Locate every Plasmodium falciparum-infected red blood cell.
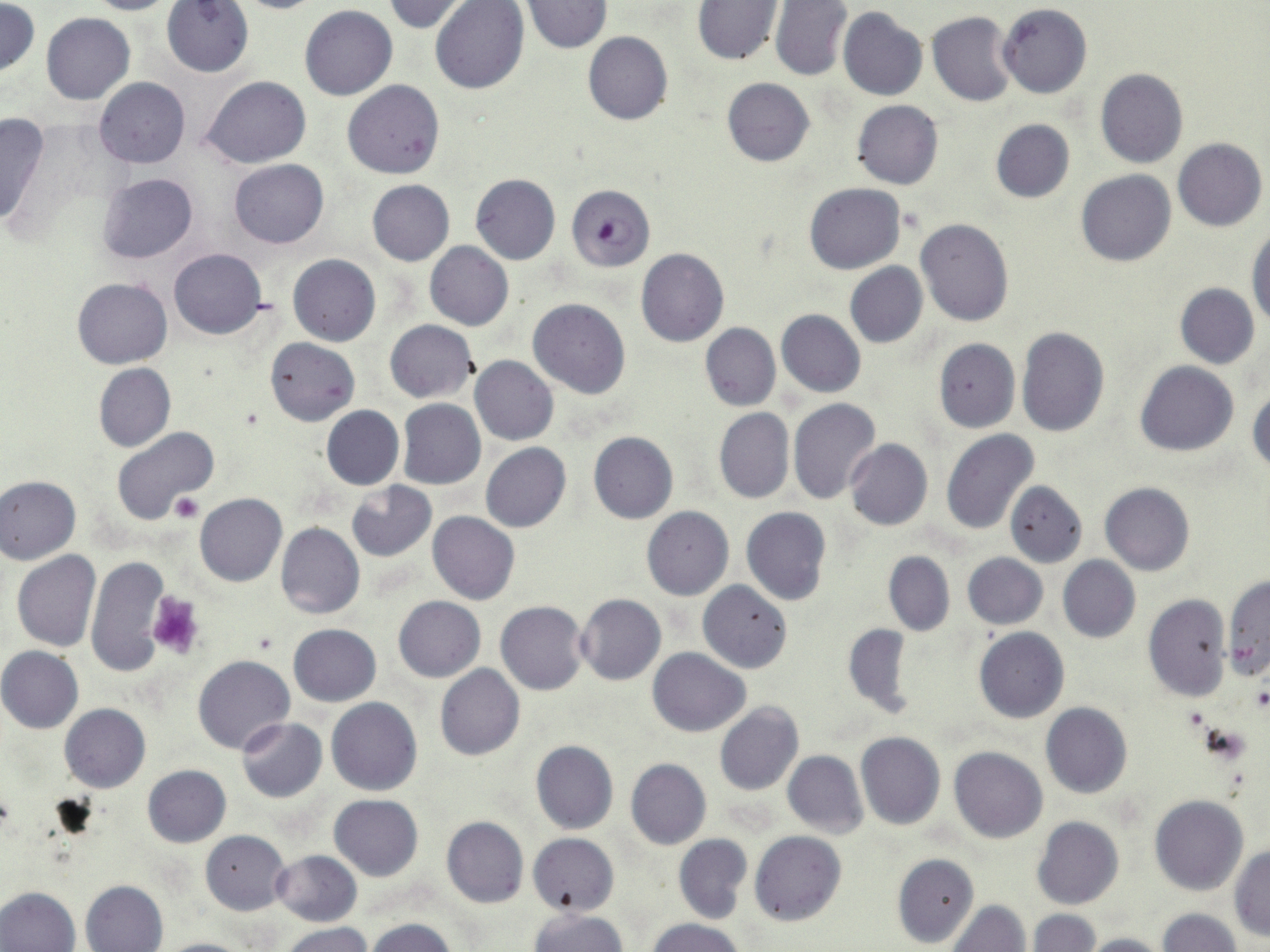

Approximate bounding boxes as [x1, y1, x2, y2] in pixels.
Plasmodium falciparum-infected red blood cells: [567, 184, 655, 272].

Summary:
  - Uninfected red blood cell locations: [81, 0, 186, 15], [221, 0, 332, 14], [381, 0, 473, 34], [161, 1, 255, 77], [769, 1, 853, 82], [432, 2, 528, 95], [521, 2, 613, 53], [693, 2, 783, 66], [1, 3, 40, 76], [998, 4, 1092, 98], [299, 5, 397, 100], [837, 7, 928, 100], [927, 11, 1018, 106], [41, 13, 135, 105], [582, 31, 673, 126], [1095, 69, 1188, 168], [202, 76, 311, 169], [93, 77, 191, 168], [722, 78, 815, 166], [343, 79, 445, 179], [851, 100, 943, 189], [0, 111, 49, 229], [990, 119, 1075, 202], [1173, 138, 1267, 231], [229, 159, 330, 248], [1075, 170, 1177, 266], [96, 173, 198, 263], [471, 174, 561, 265], [368, 180, 454, 265], [803, 182, 905, 274], [915, 219, 1014, 327], [1247, 226, 1269, 328], [425, 241, 513, 330], [168, 248, 267, 339], [636, 248, 730, 348], [288, 254, 381, 346], [845, 263, 927, 348], [73, 277, 172, 369], [1176, 283, 1259, 368], [529, 298, 630, 398], [776, 309, 866, 397], [385, 320, 478, 403], [700, 324, 780, 411], [1015, 326, 1109, 436], [265, 337, 361, 425], [933, 338, 1020, 432], [470, 356, 558, 446], [1134, 361, 1238, 456], [95, 364, 175, 451], [1248, 388, 1270, 475], [788, 398, 881, 503], [398, 400, 486, 490], [321, 406, 404, 490], [714, 408, 795, 505], [110, 426, 218, 524], [940, 429, 1039, 535], [588, 432, 678, 524], [845, 439, 933, 531], [481, 443, 571, 533], [0, 475, 82, 564], [347, 481, 437, 561], [1004, 481, 1087, 566], [1100, 483, 1194, 574], [194, 494, 287, 586], [641, 506, 732, 600], [741, 507, 832, 607], [428, 512, 521, 605], [276, 522, 365, 619], [12, 551, 100, 652], [883, 551, 956, 636], [85, 553, 172, 677], [961, 553, 1047, 629], [1058, 556, 1140, 643], [1223, 574, 1269, 683], [697, 580, 792, 673], [575, 593, 667, 685], [1143, 594, 1231, 701], [393, 596, 486, 682], [496, 601, 589, 694], [843, 623, 914, 717], [289, 624, 381, 706], [974, 627, 1068, 722], [0, 647, 84, 733], [647, 648, 750, 737], [194, 655, 295, 754], [434, 664, 525, 761], [327, 698, 422, 796], [715, 702, 804, 797], [1041, 703, 1131, 798], [60, 704, 150, 792], [236, 718, 327, 802], [856, 733, 946, 830], [531, 741, 618, 834], [949, 746, 1048, 842], [782, 751, 867, 837], [626, 759, 711, 849], [144, 766, 231, 847], [329, 794, 424, 881], [1151, 795, 1249, 896], [1032, 816, 1124, 909], [441, 817, 529, 907], [201, 830, 291, 914], [750, 830, 845, 926], [673, 833, 752, 924], [528, 834, 619, 917], [1229, 846, 1270, 941], [272, 850, 362, 926], [892, 853, 979, 949], [79, 879, 168, 952], [0, 887, 80, 952], [946, 900, 1030, 951], [1157, 909, 1240, 952], [529, 910, 630, 952], [1027, 910, 1100, 952], [646, 917, 746, 952], [366, 918, 459, 952], [280, 923, 375, 952], [1076, 933, 1169, 952], [152, 937, 257, 952]
  - Platelet locations: [168, 492, 204, 521], [146, 593, 204, 658], [1251, 686, 1270, 713]
  - Slide-level diagnosis: Plasmodium falciparum
  - Magnification: 1000x
  - Field of view: one of a larger specimen
  - Preparation: thin blood smear
  - Image size: 1270×952 pixels
  - Stain: May-Grünwald-Giemsa
  - Modality: light microscopy